Assess this cell for malaria.
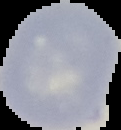

It is uninfected.

image size = 121×130 pixels
image type = cell region segmented out of the field of view; surrounding area masked to black
preparation = thin blood smear